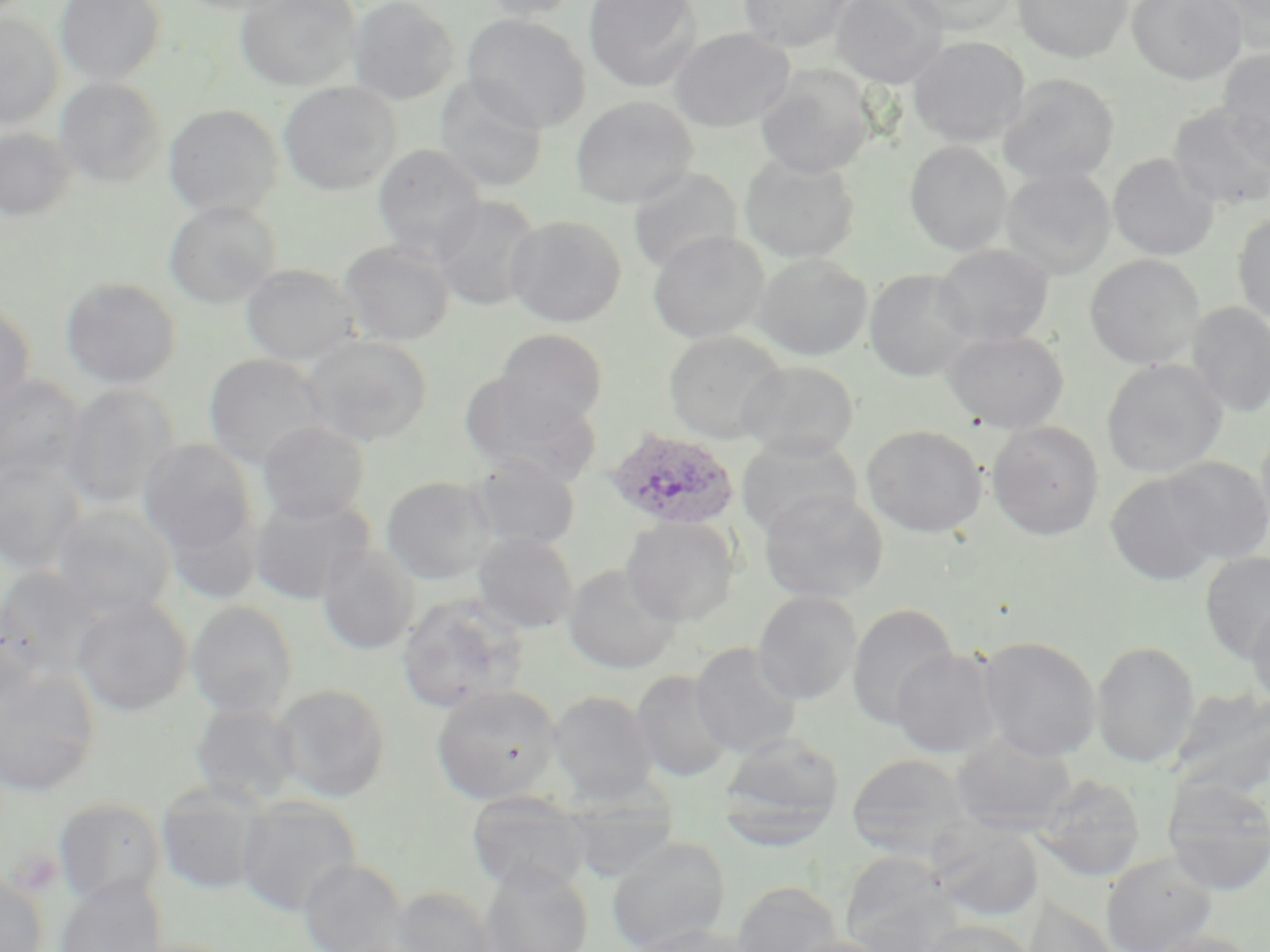
Summary:
  - Coordinate format: approximate bounding boxes as (x1,y1)-(x2,y2) corner pairs in pixels
  - Uninfected red blood cell locations: (55,0)-(166,86), (178,0)-(302,15), (236,0)-(361,91), (347,0)-(460,106), (474,0)-(586,21), (583,0)-(704,92), (738,0)-(853,52), (830,0)-(948,88), (900,0)-(1019,35), (1012,0)-(1133,63), (1128,0)-(1246,84), (1207,0)-(1270,55), (0,13)-(63,130), (462,13)-(591,132), (670,28)-(794,132), (908,36)-(1029,147), (1217,50)-(1270,168), (755,65)-(876,178), (999,73)-(1119,186), (435,77)-(549,194), (54,78)-(167,187), (278,81)-(401,195), (570,96)-(698,208), (163,104)-(283,218), (1168,105)-(1270,211), (0,127)-(76,223), (905,141)-(1012,256), (372,144)-(486,260), (740,153)-(860,262), (1108,153)-(1219,260), (627,166)-(744,274), (1001,167)-(1116,279), (431,194)-(542,312), (163,201)-(281,308), (1232,210)-(1270,326), (506,215)-(627,327), (648,230)-(769,344), (339,239)-(455,346), (933,243)-(1053,346), (753,253)-(872,360), (1084,254)-(1205,370), (240,263)-(361,366), (864,269)-(978,381), (60,276)-(182,389), (1187,302)-(1270,417), (0,304)-(36,416), (495,329)-(609,429), (663,329)-(787,444), (942,330)-(1069,433), (299,334)-(433,447), (204,353)-(329,469), (1101,358)-(1228,478), (737,360)-(861,460), (460,372)-(602,487), (0,375)-(86,484), (60,384)-(180,509), (257,421)-(370,524), (986,421)-(1105,540), (862,425)-(987,537), (1256,426)-(1270,536), (736,435)-(862,539), (138,439)-(259,558), (468,454)-(580,552), (1,456)-(87,576), (1162,456)-(1270,563), (1105,471)-(1224,585), (381,476)-(497,583), (758,488)-(888,604), (249,494)-(375,605), (51,504)-(178,620), (160,504)-(262,606), (621,516)-(740,626), (471,532)-(579,634), (316,542)-(420,655), (1199,550)-(1270,663), (563,564)-(681,674), (0,566)-(111,679), (753,591)-(863,705), (395,593)-(528,714), (72,596)-(193,717), (1246,597)-(1270,709), (186,601)-(298,717), (847,602)-(958,730), (0,613)-(43,716), (978,636)-(1101,760), (1091,640)-(1200,767), (689,642)-(803,758), (891,647)-(1004,758), (0,665)-(101,799), (631,671)-(733,782), (271,683)-(391,802), (431,684)-(562,804), (1170,686)-(1270,801), (548,691)-(658,804), (191,701)-(302,809), (720,733)-(845,848), (950,733)-(1078,835), (846,753)-(974,859), (1031,773)-(1145,882), (1161,780)-(1270,895), (562,783)-(683,880), (155,784)-(267,895), (466,790)-(591,896), (236,796)-(362,917), (52,797)-(167,907), (929,820)-(1043,921), (606,835)-(731,952), (840,850)-(957,950), (1101,852)-(1217,952), (299,858)-(408,952), (480,863)-(592,952), (0,871)-(48,952), (53,876)-(166,952), (731,880)-(844,952), (387,885)-(502,952), (1022,896)-(1119,952), (921,919)-(1036,952), (626,923)-(757,952), (1141,930)-(1262,952), (780,936)-(894,952)
  - Plasmodium ovale-infected red blood cell locations: (604,427)-(740,530)
  - Platelet locations: (10,849)-(63,896)
  - Slide-level diagnosis: Plasmodium ovale
  - Stain: May-Grünwald-Giemsa
  - Image size: 1270×952 pixels
  - Modality: light microscopy
  - Preparation: thin blood smear
  - Field of view: single
  - Magnification: 1000x